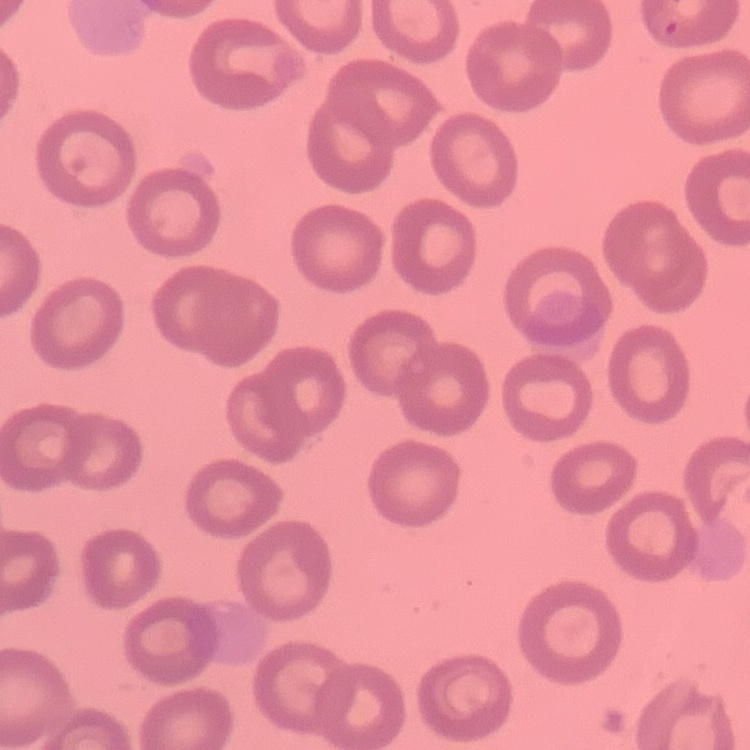

Summary:
  - Erythrocyte morphology: no rouleaux formation
  - Preparation: thin blood film
  - Image type: one tile cut from a larger photomicrograph
  - Stain: Field's or Giemsa